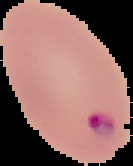
Summary:
  - Image type: cell region segmented out of the field of view; surrounding area masked to black
  - Image size: 133×166 pixels
  - Preparation: thin blood smear
  - Result: Plasmodium parasites identified